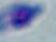
Toxoplasma gondii is seen. Photomicrograph. Captured at 1000x magnification.